Give the extent of all uninfected red blood cells.
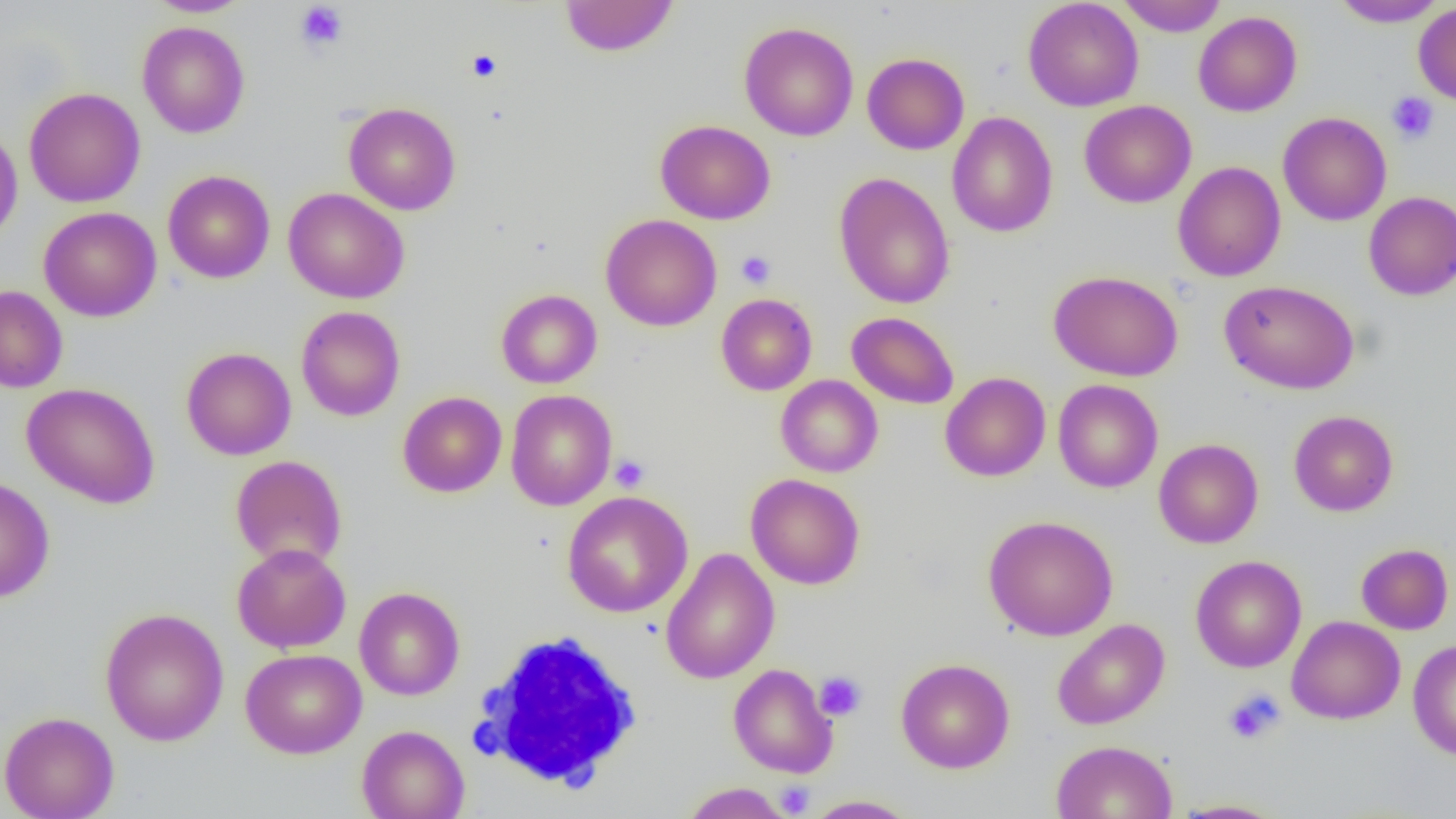

Approximate bounding boxes as (x1, y1, x2, y2) in pixels.
Uninfected red blood cells: (145, 0, 253, 17), (559, 0, 679, 57), (1022, 0, 1144, 112), (1117, 0, 1228, 36), (1330, 0, 1448, 27), (1413, 3, 1456, 105), (1193, 11, 1302, 117), (137, 21, 250, 138), (739, 21, 858, 141), (862, 52, 969, 155), (24, 87, 145, 207), (1079, 100, 1196, 208), (343, 102, 461, 215), (947, 111, 1058, 238), (1278, 112, 1392, 226), (655, 119, 775, 224), (0, 126, 23, 244), (1172, 161, 1286, 281), (163, 170, 275, 283), (833, 172, 955, 309), (283, 187, 410, 304), (1363, 192, 1456, 300), (39, 207, 161, 321), (600, 213, 722, 332), (1048, 270, 1183, 382), (1220, 280, 1359, 394), (0, 285, 68, 393), (496, 289, 602, 389), (716, 293, 817, 395), (296, 306, 406, 421), (846, 311, 959, 409), (181, 347, 296, 461), (940, 372, 1051, 481), (776, 375, 883, 477), (1053, 378, 1163, 493), (21, 382, 160, 509), (505, 390, 617, 510), (397, 391, 507, 497), (1289, 410, 1398, 516), (1153, 438, 1264, 548), (231, 454, 347, 569), (745, 473, 865, 590), (0, 476, 55, 603), (562, 490, 693, 618), (983, 515, 1119, 641), (232, 543, 351, 653), (1356, 543, 1454, 634), (660, 547, 779, 684), (1190, 555, 1307, 673), (354, 586, 464, 700), (100, 607, 229, 747), (1286, 615, 1405, 724), (1052, 618, 1170, 730), (1408, 640, 1456, 759), (240, 648, 367, 759), (895, 657, 1015, 774), (728, 663, 838, 778), (0, 711, 119, 819), (357, 725, 469, 819), (1051, 739, 1178, 819), (680, 782, 792, 818), (803, 795, 920, 818), (1170, 799, 1286, 818).

Platelet locations: (294, 2, 349, 52), (467, 50, 501, 82), (1386, 92, 1439, 143), (736, 251, 776, 289), (610, 454, 650, 492), (814, 671, 867, 721), (1223, 688, 1286, 745), (775, 781, 815, 817). White blood cell locations: (469, 630, 644, 791). Slide-level diagnosis: negative for blood parasites. Image is 1456×819 pixels. Thin blood smear. Captured at 1000x magnification. Light microscopy. One field of a larger specimen.